Locate every P. falciparum parasite and identify its life-cycle stage.
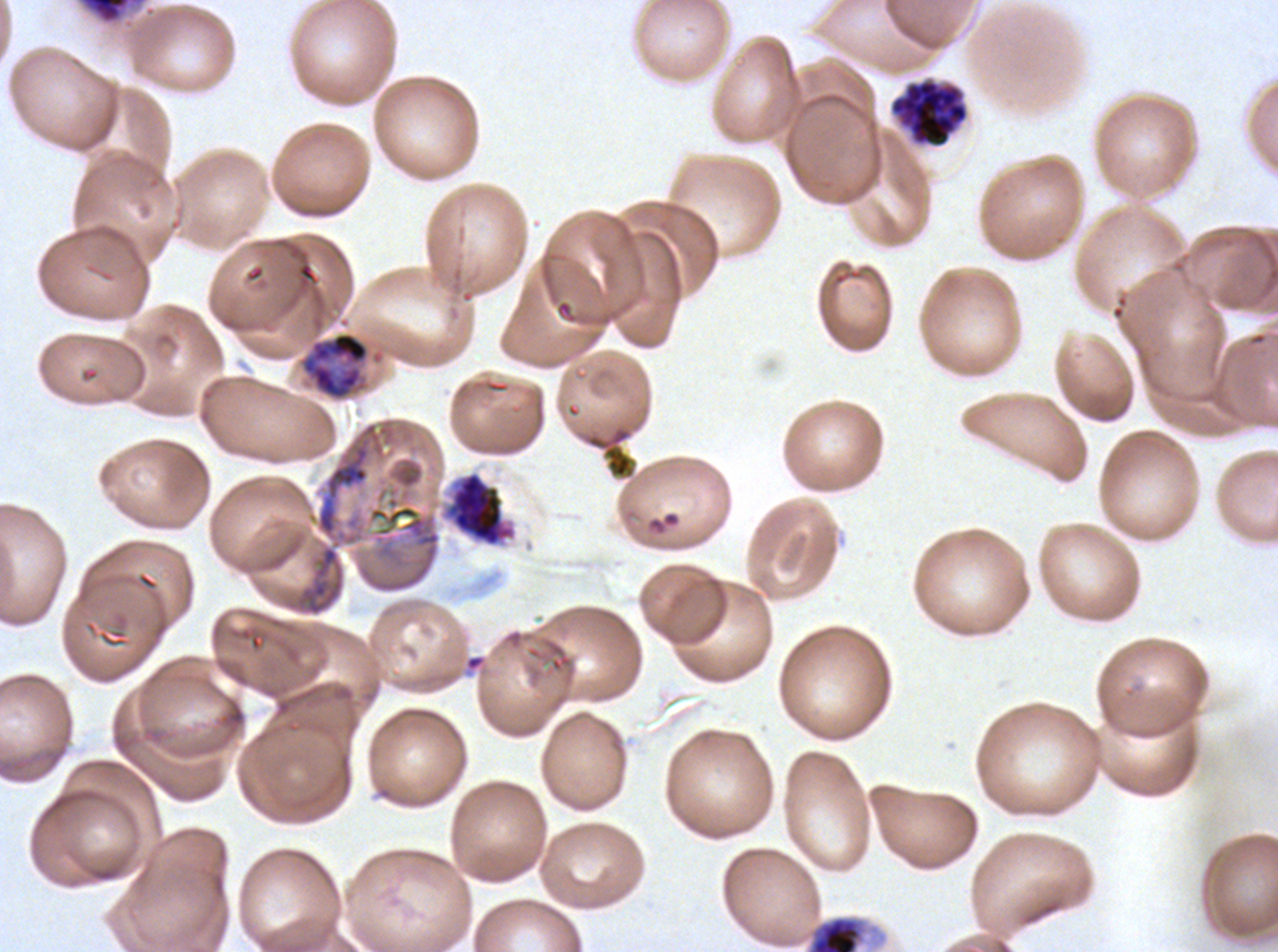

Approximate bounding boxes as (x1, y1, x2, y2) in pixels.
Early schizonts: (78, 0, 146, 25), (301, 331, 370, 400).
Segmenters: (890, 79, 969, 148), (440, 470, 518, 548).
No rings, late-ring/early-trophozoite forms, mid trophozoites, late trophozoites, late schizonts, or gametocytes observed.

Debris locations: (581, 423, 637, 481), (805, 914, 888, 951). Ex-vivo P. falciparum culture from a patient in The Gambia, grown for 24 to 48 hours. Thin blood smear. One sub-image of a larger composite. Image is 1278×952 pixels. Life-cycle stages observed: early schizont, segmenter. Giemsa-stained preparation.